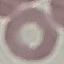

malaria status = uninfected
stain = Giemsa
image type = automatically extracted cell patch, resized to 64 × 64 pixels
preparation = thin blood smear
capture = smartphone camera at the microscope eyepiece